Classify this cell by malaria status.
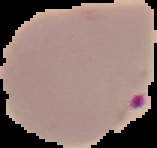
Parasitized.

image_size: 157×148 pixels
preparation: thin blood smear
image_type: segmented cell region with the area outside set to black